Report the malaria status of this cell.
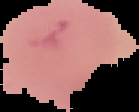
It is uninfected.

Image is 139×112 pixels. From a thin blood smear. Cell region segmented out of the field of view; the surrounding area is masked to black.